Classify this cell by malaria status.
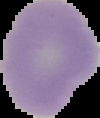

It is uninfected.

Image is 100×118 pixels. From a thin blood film. Cell region segmented out of the field of view; the surrounding area is masked to black.